Name the parasite shown.
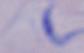
A trypanosome.

1000x magnification. Micrograph.